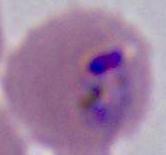

A Plasmodium parasite is seen. Photomicrograph. 400x or 1000x magnification.